Classify this cell by malaria status.
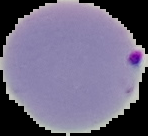
It is parasitized.

image size = 148×136 pixels
preparation = thin blood film
image type = segmented cell region on a black background